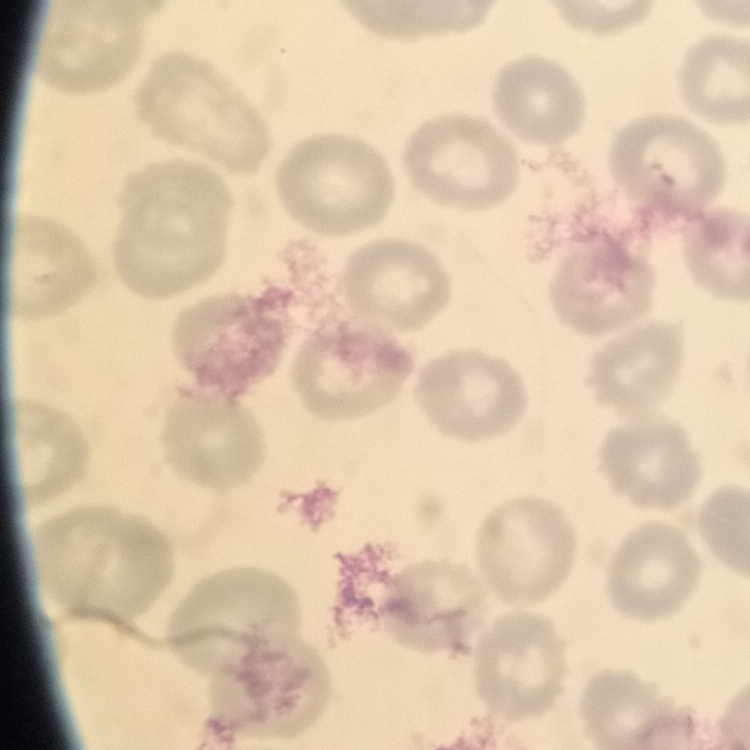

Summary:
  - Erythrocyte morphology: no rouleaux formation
  - Preparation: thin blood film
  - Stain: Field's or Giemsa
  - Image type: square crop of a larger photomicrograph